State the blood parasite species.
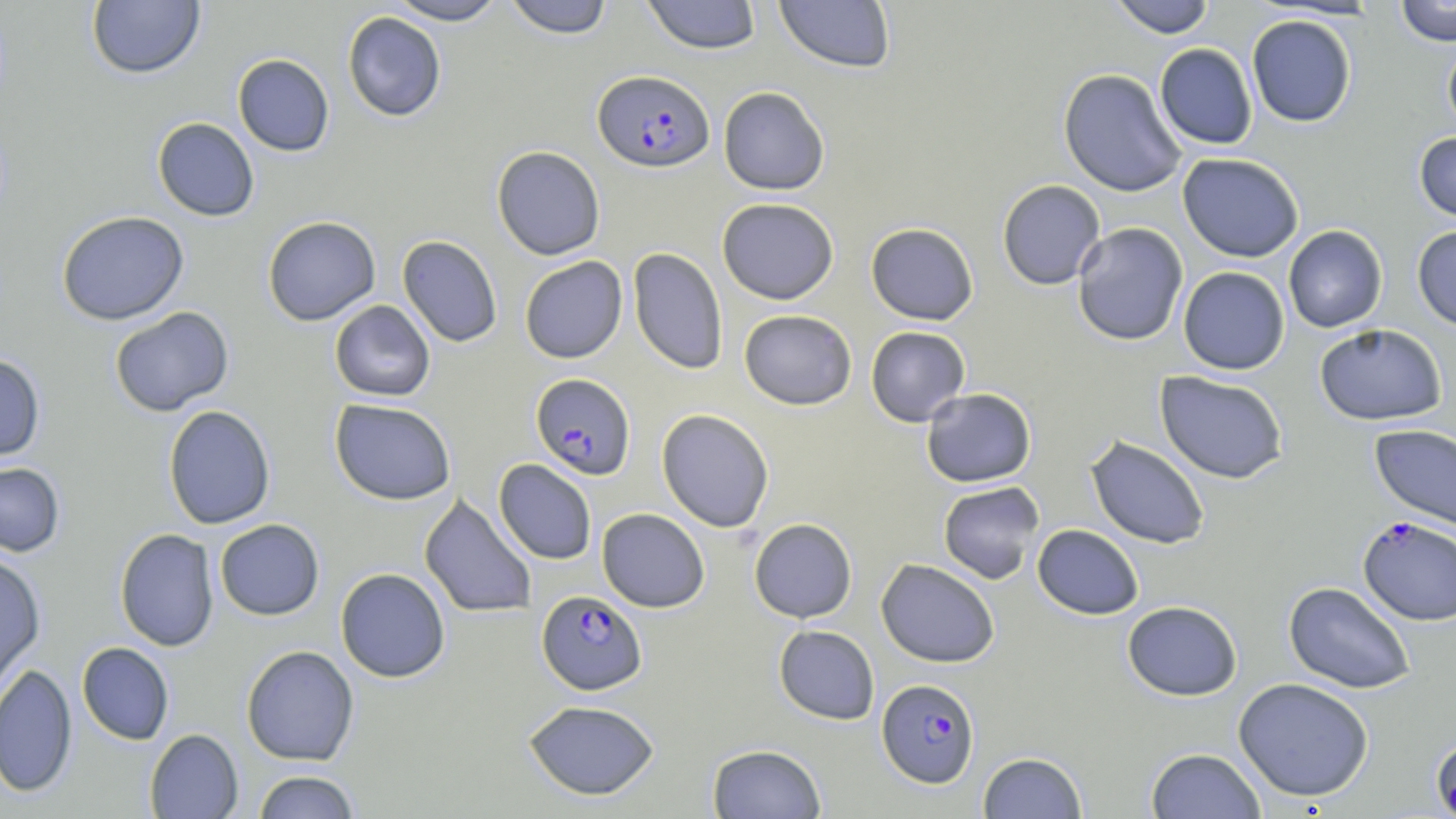
Plasmodium falciparum.

Summary:
  - Coordinate format: approximate bounding boxes as named x1/y1/x2/y2 corners in pixels
  - Plasmodium falciparum-infected red blood cell locations: (x1=592, y1=70, x2=715, y2=173), (x1=530, y1=373, x2=636, y2=480), (x1=1357, y1=516, x2=1456, y2=626), (x1=537, y1=590, x2=647, y2=695), (x1=877, y1=678, x2=980, y2=787)
  - Uninfected red blood cell locations: (x1=86, y1=0, x2=205, y2=79), (x1=386, y1=0, x2=507, y2=24), (x1=502, y1=0, x2=616, y2=38), (x1=642, y1=0, x2=762, y2=54), (x1=774, y1=0, x2=896, y2=73), (x1=1107, y1=0, x2=1216, y2=38), (x1=1395, y1=0, x2=1456, y2=46), (x1=342, y1=11, x2=447, y2=122), (x1=1246, y1=14, x2=1357, y2=127), (x1=1442, y1=36, x2=1456, y2=139), (x1=1154, y1=43, x2=1258, y2=149), (x1=233, y1=53, x2=334, y2=156), (x1=1058, y1=68, x2=1187, y2=197), (x1=718, y1=86, x2=830, y2=195), (x1=152, y1=117, x2=259, y2=221), (x1=1414, y1=132, x2=1456, y2=224), (x1=491, y1=145, x2=606, y2=260), (x1=1177, y1=152, x2=1304, y2=262), (x1=997, y1=179, x2=1106, y2=290), (x1=717, y1=198, x2=839, y2=304), (x1=56, y1=210, x2=189, y2=325), (x1=262, y1=216, x2=381, y2=326), (x1=865, y1=222, x2=979, y2=325), (x1=1072, y1=222, x2=1188, y2=346), (x1=1283, y1=225, x2=1387, y2=333), (x1=1412, y1=225, x2=1456, y2=332), (x1=397, y1=235, x2=502, y2=348), (x1=628, y1=247, x2=728, y2=375), (x1=519, y1=256, x2=628, y2=363), (x1=1178, y1=267, x2=1290, y2=375), (x1=329, y1=300, x2=435, y2=401), (x1=109, y1=306, x2=234, y2=416), (x1=739, y1=309, x2=857, y2=410), (x1=1314, y1=324, x2=1447, y2=426), (x1=865, y1=326, x2=970, y2=426), (x1=0, y1=352, x2=46, y2=461), (x1=1155, y1=370, x2=1289, y2=484), (x1=920, y1=388, x2=1037, y2=487), (x1=329, y1=398, x2=457, y2=505), (x1=162, y1=404, x2=276, y2=529), (x1=656, y1=408, x2=774, y2=533), (x1=1369, y1=424, x2=1456, y2=531), (x1=1085, y1=435, x2=1211, y2=550), (x1=494, y1=459, x2=597, y2=564), (x1=0, y1=461, x2=66, y2=558), (x1=937, y1=481, x2=1045, y2=585), (x1=419, y1=493, x2=537, y2=619), (x1=597, y1=508, x2=710, y2=612), (x1=749, y1=518, x2=857, y2=623), (x1=214, y1=519, x2=324, y2=620), (x1=1032, y1=524, x2=1144, y2=620), (x1=114, y1=528, x2=219, y2=652), (x1=0, y1=552, x2=46, y2=690), (x1=876, y1=558, x2=1000, y2=668), (x1=336, y1=568, x2=450, y2=683), (x1=1283, y1=581, x2=1417, y2=695), (x1=1122, y1=600, x2=1243, y2=701), (x1=773, y1=625, x2=879, y2=724), (x1=77, y1=642, x2=174, y2=745), (x1=241, y1=645, x2=359, y2=766), (x1=0, y1=663, x2=78, y2=797), (x1=1233, y1=677, x2=1375, y2=803), (x1=522, y1=699, x2=660, y2=800), (x1=145, y1=729, x2=243, y2=818), (x1=1429, y1=732, x2=1456, y2=819), (x1=707, y1=743, x2=827, y2=819), (x1=1146, y1=747, x2=1266, y2=819), (x1=978, y1=751, x2=1088, y2=818), (x1=252, y1=770, x2=361, y2=818)
  - Image size: 1456×819 pixels
  - Field of view: single
  - Magnification: 1000x
  - Modality: light microscopy
  - Preparation: thin blood film
  - Stain: May-Grünwald-Giemsa